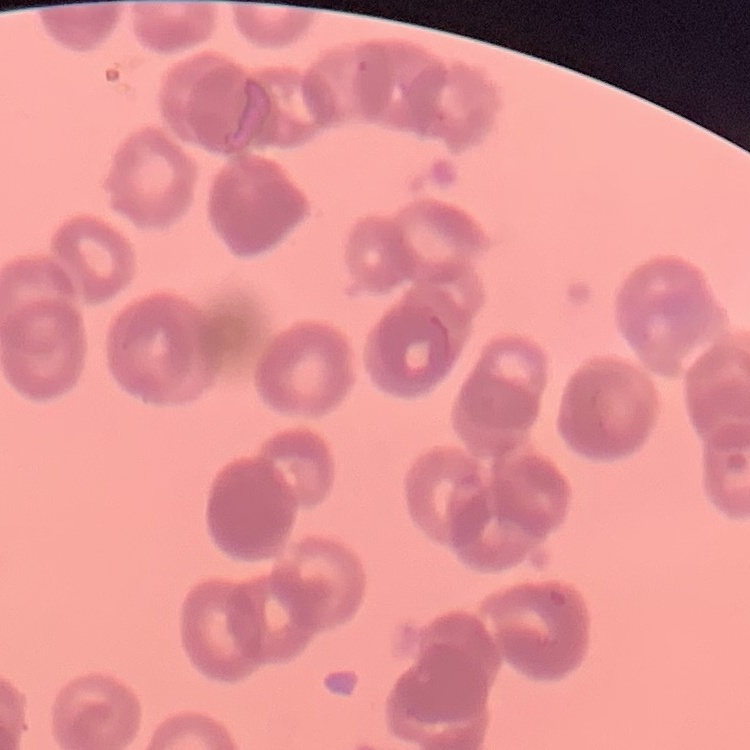

The erythrocytes show rouleaux formation. One tile cut from a larger photomicrograph. Field's or Giemsa stain. Thin blood film.